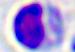
Captured at 400x magnification. A leukocyte is seen. Micrograph.